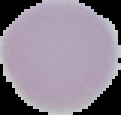

result = no malaria parasites detected
image size = 121×115 pixels
preparation = thin blood film
image type = segmented cell region with the area outside set to black